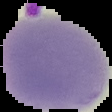

{
  "result": "negative for Plasmodium parasites",
  "image_size": "112×112 pixels",
  "preparation": "thin blood smear",
  "image_type": "segmented cell region with the area outside set to black"
}